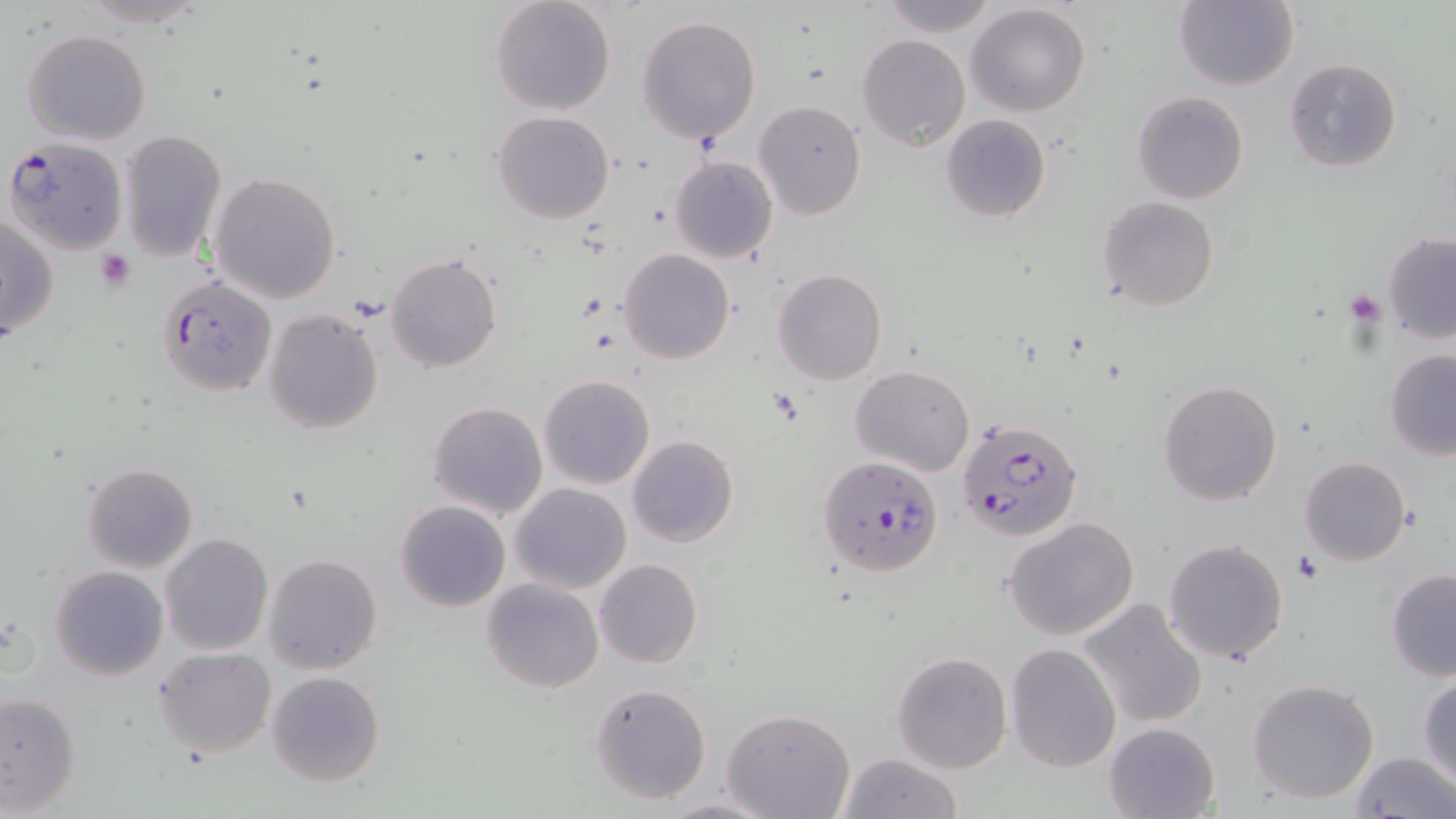
slide-level diagnosis = Plasmodium falciparum
preparation = thin blood smear
field of view = one of a larger specimen
magnification = 1000x
Plasmodium falciparum-infected red blood cell locations = approximate bounding boxes as (x1, y1, x2, y2) in pixels: (3, 135, 128, 255), (157, 276, 277, 397), (955, 415, 1084, 540), (815, 454, 945, 577)
platelet locations = approximate bounding boxes as (x1, y1, x2, y2) in pixels: (96, 250, 136, 294), (1342, 289, 1387, 326), (1293, 555, 1320, 584)
stain = May-Grünwald-Giemsa
modality = light microscopy
image size = 1456×819 pixels
uninfected red blood cell locations = approximate bounding boxes as (x1, y1, x2, y2) in pixels: (72, 0, 217, 29), (489, 0, 617, 115), (875, 0, 999, 36), (1172, 1, 1299, 90), (964, 3, 1091, 116), (637, 14, 762, 144), (23, 29, 152, 145), (856, 34, 970, 152), (1283, 57, 1403, 173), (1132, 90, 1250, 205), (754, 100, 866, 219), (492, 111, 615, 225), (940, 115, 1052, 223), (118, 130, 227, 262), (670, 155, 778, 263), (210, 170, 342, 304), (1097, 196, 1218, 311), (2, 213, 60, 342), (1382, 232, 1456, 344), (617, 248, 737, 364), (387, 251, 503, 372), (771, 267, 888, 385), (262, 308, 384, 435), (1384, 349, 1456, 458), (850, 364, 975, 477), (537, 374, 656, 490), (1156, 378, 1285, 505), (426, 400, 547, 520), (627, 434, 739, 548), (1300, 455, 1411, 565), (81, 461, 198, 572), (511, 483, 631, 595), (395, 499, 510, 612), (1003, 518, 1139, 642), (159, 533, 272, 656), (1162, 538, 1291, 665), (264, 554, 383, 675), (595, 559, 703, 669), (49, 565, 170, 681), (1385, 568, 1456, 680), (482, 578, 603, 693), (1078, 599, 1208, 729), (1004, 642, 1121, 772), (153, 646, 276, 758), (891, 651, 1012, 774), (266, 671, 385, 789), (1418, 673, 1456, 787), (1247, 677, 1380, 805), (589, 682, 712, 805), (0, 690, 82, 814), (722, 708, 855, 819), (1103, 721, 1221, 819), (1350, 750, 1456, 819), (838, 753, 963, 818), (659, 796, 776, 819)